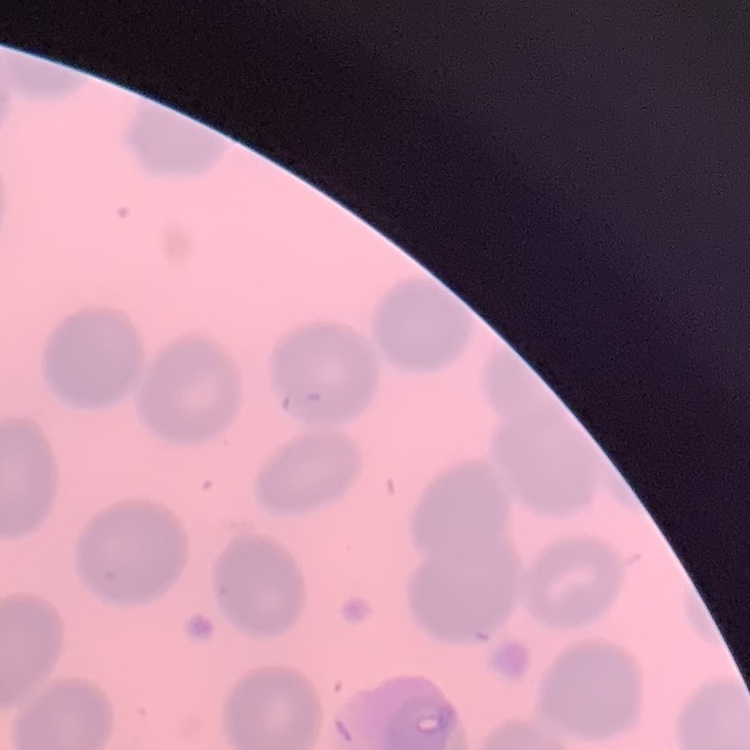

Summary:
  - Erythrocyte morphology: no rouleaux formation
  - Image type: square crop of a larger photomicrograph
  - Stain: Field's or Giemsa
  - Preparation: thin blood film